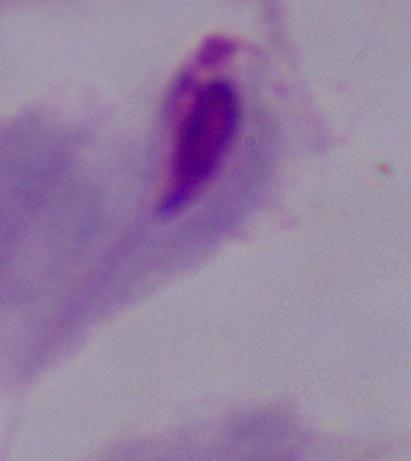

Summary:
  - Magnification: 1000x
  - Identification: trichomonad
  - Modality: photomicrograph